Identify the parasite.
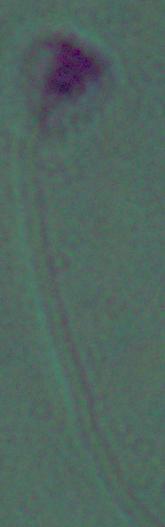

This is Leishmania.

1000x magnification. Photomicrograph.